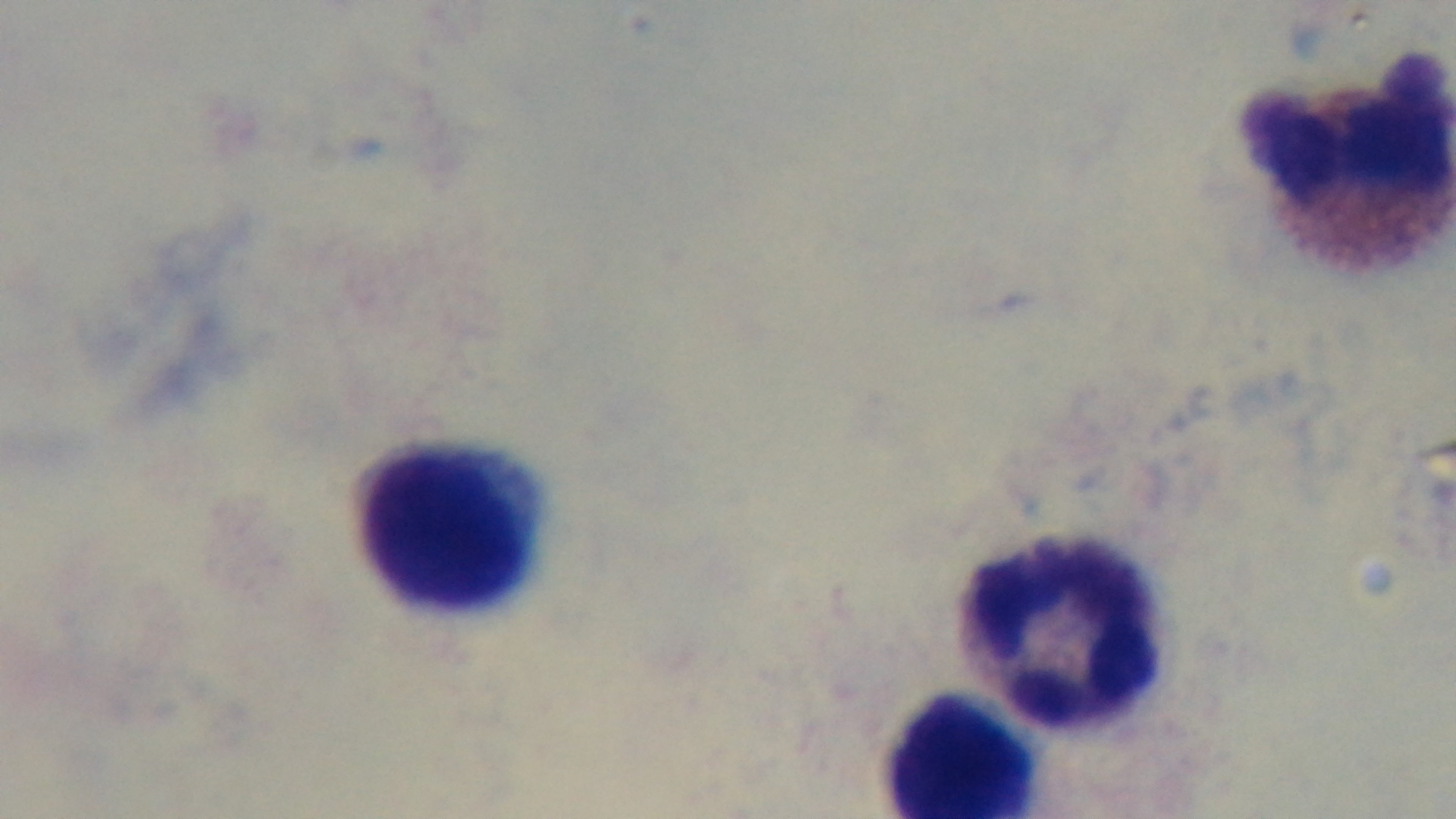
Oil-immersion objective, 100x. Mounted 4K digital camera. Preparation: thick blood film. Photomicrograph. Giemsa-stained. Single field of view. Malaria status: uninfected.